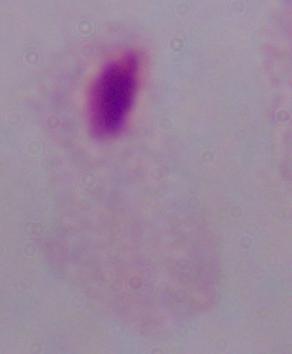
identification = trichomonad
magnification = 1000x
modality = photomicrograph